Report the malaria status of this cell.
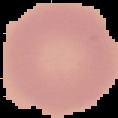

Uninfected.

Image is 118×118 pixels. Segmented cell region on a black background. From a thin blood smear.